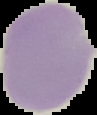
Summary:
  - Preparation: thin blood smear
  - Image type: segmented cell region with the area outside set to black
  - Malaria status: uninfected
  - Image size: 97×115 pixels